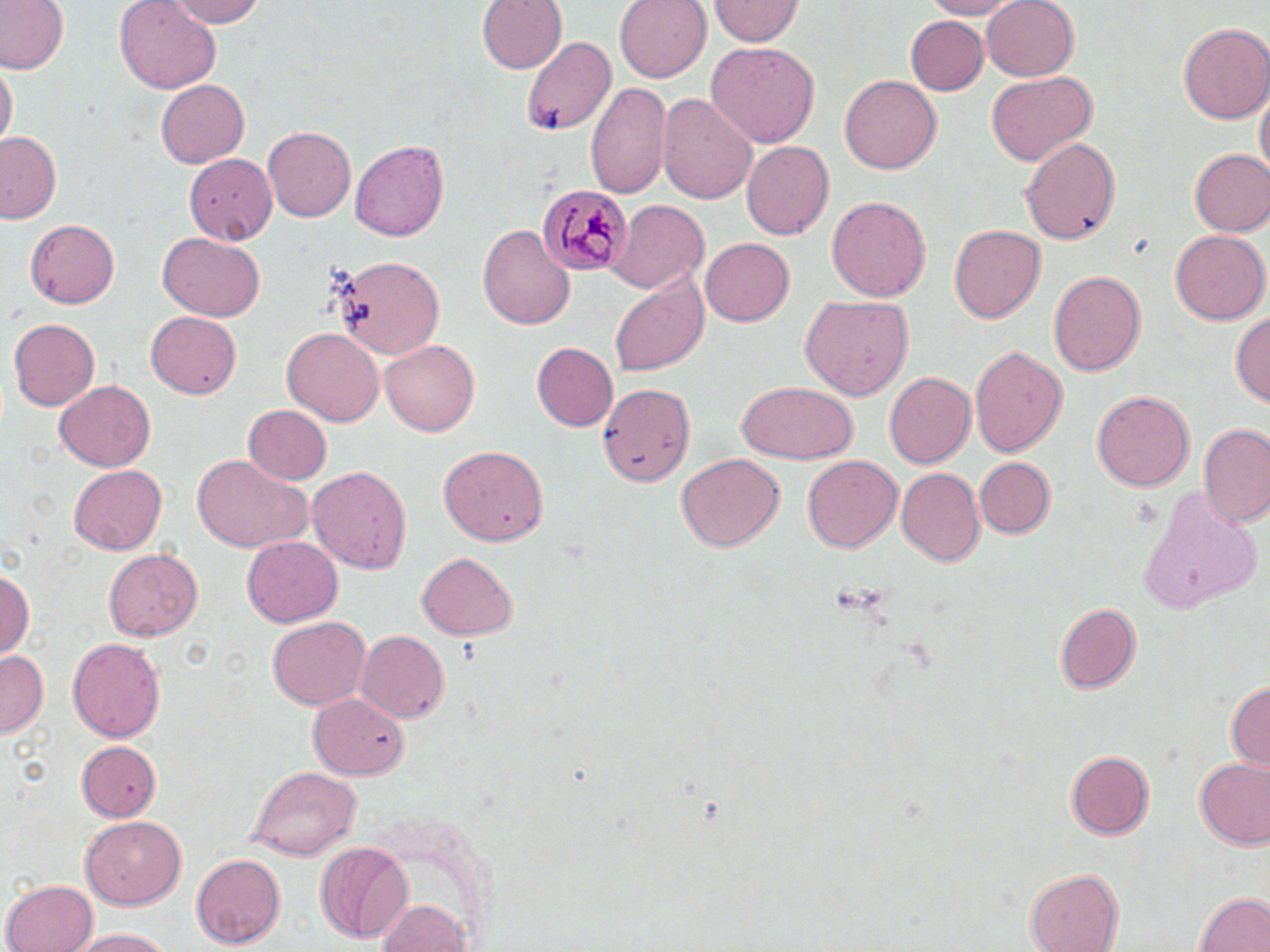
Summary:
  - Coordinate format: approximate bounding boxes as (x1,y1)-(x2,y2) corner pairs in pixels
  - Plasmodium malariae-infected red blood cell locations: (540,181)-(632,275)
  - Uninfected red blood cell locations: (0,0)-(68,75), (116,0)-(220,90), (161,0)-(271,27), (477,0)-(566,76), (613,0)-(711,81), (709,0)-(802,45), (924,0)-(1020,20), (982,0)-(1080,79), (704,11)-(807,78), (903,16)-(988,94), (1178,21)-(1269,122), (521,35)-(615,137), (706,42)-(822,147), (0,64)-(15,153), (983,71)-(1096,165), (839,74)-(941,176), (154,79)-(247,167), (587,80)-(672,201), (1255,90)-(1268,179), (659,92)-(757,206), (264,124)-(355,219), (1,132)-(63,224), (1020,137)-(1121,247), (740,138)-(834,237), (350,140)-(450,242), (1189,148)-(1270,236), (181,152)-(277,241), (828,196)-(930,303), (608,200)-(707,293), (25,218)-(119,309), (480,223)-(575,332), (949,223)-(1045,323), (1170,229)-(1268,325), (159,232)-(265,320), (699,238)-(794,327), (335,255)-(445,358), (1047,267)-(1145,376), (609,272)-(709,378), (798,294)-(912,400), (1232,309)-(1268,413), (145,311)-(243,398), (8,315)-(99,409), (282,328)-(384,426), (381,337)-(482,435), (533,343)-(617,431), (967,343)-(1067,458), (883,371)-(975,471), (593,380)-(700,488), (736,380)-(859,465), (54,382)-(153,472), (1091,390)-(1195,493), (240,404)-(331,484), (1199,424)-(1270,527), (437,446)-(552,546), (189,454)-(313,554), (676,454)-(784,553), (802,455)-(901,554), (972,456)-(1054,538), (309,463)-(409,577), (69,465)-(167,554), (898,468)-(985,568), (1140,492)-(1262,610), (241,536)-(342,628), (102,548)-(201,642), (418,551)-(519,638), (3,565)-(35,660), (1055,602)-(1144,693), (265,616)-(371,711), (356,630)-(449,724), (67,635)-(166,743), (0,651)-(47,741), (1226,681)-(1269,774), (309,693)-(407,779), (78,740)-(162,822), (1064,745)-(1155,840), (1195,757)-(1270,850), (248,766)-(358,860), (83,817)-(184,910), (313,843)-(414,944), (193,853)-(285,947), (1024,867)-(1123,951), (2,877)-(98,952), (1194,890)-(1269,952), (377,898)-(468,951), (71,927)-(177,950)
  - Slide-level diagnosis: Plasmodium malariae
  - Image size: 1270×952 pixels
  - Preparation: thin blood film
  - Magnification: 1000x
  - Modality: light microscopy
  - Field of view: one of a larger specimen
  - Stain: May-Grünwald-Giemsa